State the blood parasite species.
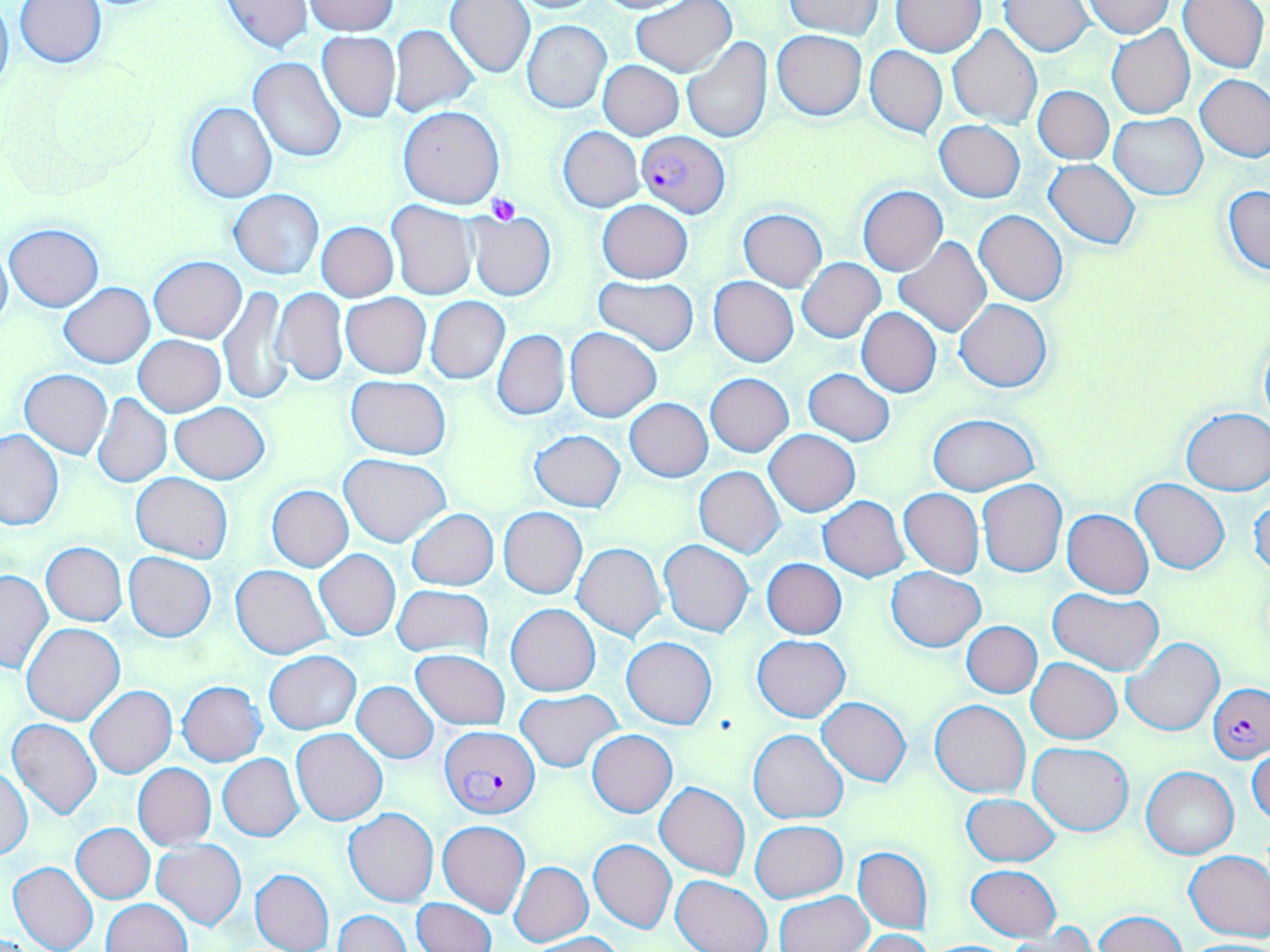
Plasmodium falciparum.

modality = light microscopy
stain = May-Grünwald-Giemsa
Plasmodium falciparum-infected red blood cell locations = approximate bounding boxes as (x1, y1, x2, y2) in pixels: (636, 131, 731, 217), (1207, 683, 1270, 764), (439, 726, 541, 818)
magnification = 1000x
image size = 1270×952 pixels
uninfected red blood cell locations = approximate bounding boxes as (x1, y1, x2, y2) in pixels: (0, 0, 15, 98), (219, 0, 313, 53), (589, 0, 699, 13), (631, 0, 738, 76), (783, 0, 887, 39), (892, 0, 987, 56), (1178, 0, 1269, 73), (14, 1, 106, 69), (304, 1, 397, 35), (444, 1, 535, 77), (508, 1, 606, 13), (1082, 1, 1174, 38), (999, 2, 1095, 56), (523, 20, 613, 115), (389, 24, 479, 117), (947, 25, 1041, 127), (1106, 25, 1194, 119), (772, 30, 868, 120), (316, 31, 400, 123), (681, 36, 772, 145), (865, 46, 947, 138), (248, 57, 346, 162), (598, 60, 683, 139), (1196, 74, 1269, 161), (1033, 85, 1114, 163), (184, 100, 277, 203), (398, 105, 505, 208), (1109, 113, 1208, 200), (934, 121, 1025, 202), (558, 127, 643, 212), (1044, 159, 1141, 249), (1222, 183, 1270, 277), (857, 186, 947, 275), (228, 190, 326, 279), (387, 200, 477, 300), (598, 200, 693, 282), (738, 208, 828, 292), (467, 210, 556, 301), (975, 210, 1067, 306), (316, 221, 398, 301), (4, 223, 103, 310), (894, 237, 992, 338), (0, 241, 12, 337), (149, 256, 245, 342), (798, 257, 886, 342), (591, 276, 700, 355), (709, 277, 799, 367), (59, 281, 155, 368), (219, 286, 293, 406), (272, 287, 349, 386), (341, 293, 431, 378), (425, 296, 509, 384), (956, 299, 1052, 392), (856, 307, 942, 398), (566, 328, 660, 421), (492, 329, 570, 420), (1258, 331, 1270, 433), (133, 335, 225, 417), (19, 368, 112, 459), (803, 369, 896, 445), (705, 373, 794, 455), (346, 375, 450, 458), (93, 393, 171, 487), (624, 398, 713, 481), (170, 402, 269, 483), (1179, 407, 1270, 494), (928, 414, 1040, 496), (0, 428, 66, 530), (529, 429, 626, 511), (765, 430, 860, 517), (340, 454, 451, 547), (694, 466, 786, 558), (131, 472, 234, 563), (977, 480, 1067, 577), (1131, 480, 1229, 575), (266, 485, 354, 572), (899, 488, 984, 578), (1249, 492, 1270, 581), (818, 496, 911, 580), (498, 507, 587, 597), (407, 508, 499, 591), (1062, 508, 1153, 597), (658, 540, 753, 637), (41, 542, 127, 625), (573, 542, 668, 640), (315, 549, 400, 640), (124, 552, 215, 641), (762, 559, 846, 638), (231, 565, 331, 660), (886, 567, 985, 651), (0, 569, 52, 673), (393, 585, 492, 660), (1048, 588, 1163, 674), (506, 603, 600, 696), (963, 621, 1042, 697), (22, 623, 125, 725), (752, 635, 851, 721), (622, 636, 716, 729), (1122, 636, 1223, 735), (264, 650, 361, 734), (410, 650, 511, 729), (1027, 658, 1122, 743), (177, 681, 267, 767), (352, 681, 439, 763), (85, 686, 177, 779), (516, 691, 621, 771), (817, 697, 912, 786), (929, 700, 1031, 799), (7, 718, 102, 819), (291, 728, 388, 825), (749, 729, 847, 823), (586, 730, 677, 817), (1028, 743, 1134, 835), (1248, 745, 1270, 826), (217, 753, 304, 841), (132, 762, 217, 850), (1, 765, 32, 860), (1141, 766, 1239, 859), (656, 781, 750, 879), (962, 794, 1061, 867), (343, 808, 439, 907), (750, 819, 848, 903), (437, 820, 530, 917), (72, 823, 155, 902), (588, 839, 677, 933), (153, 840, 246, 930), (854, 845, 933, 935), (1185, 849, 1270, 941), (8, 861, 99, 952), (509, 861, 594, 947), (967, 865, 1060, 940), (250, 868, 334, 952), (672, 875, 772, 952), (775, 892, 873, 952), (412, 897, 495, 952), (100, 899, 192, 951), (333, 910, 411, 952), (1095, 910, 1186, 951), (1005, 926, 1098, 951), (855, 929, 933, 952), (531, 932, 623, 951)
preparation = thin blood film
field of view = single
platelet locations = approximate bounding boxes as (x1, y1, x2, y2) in pixels: (486, 195, 521, 225)